Identify the blood parasite species.
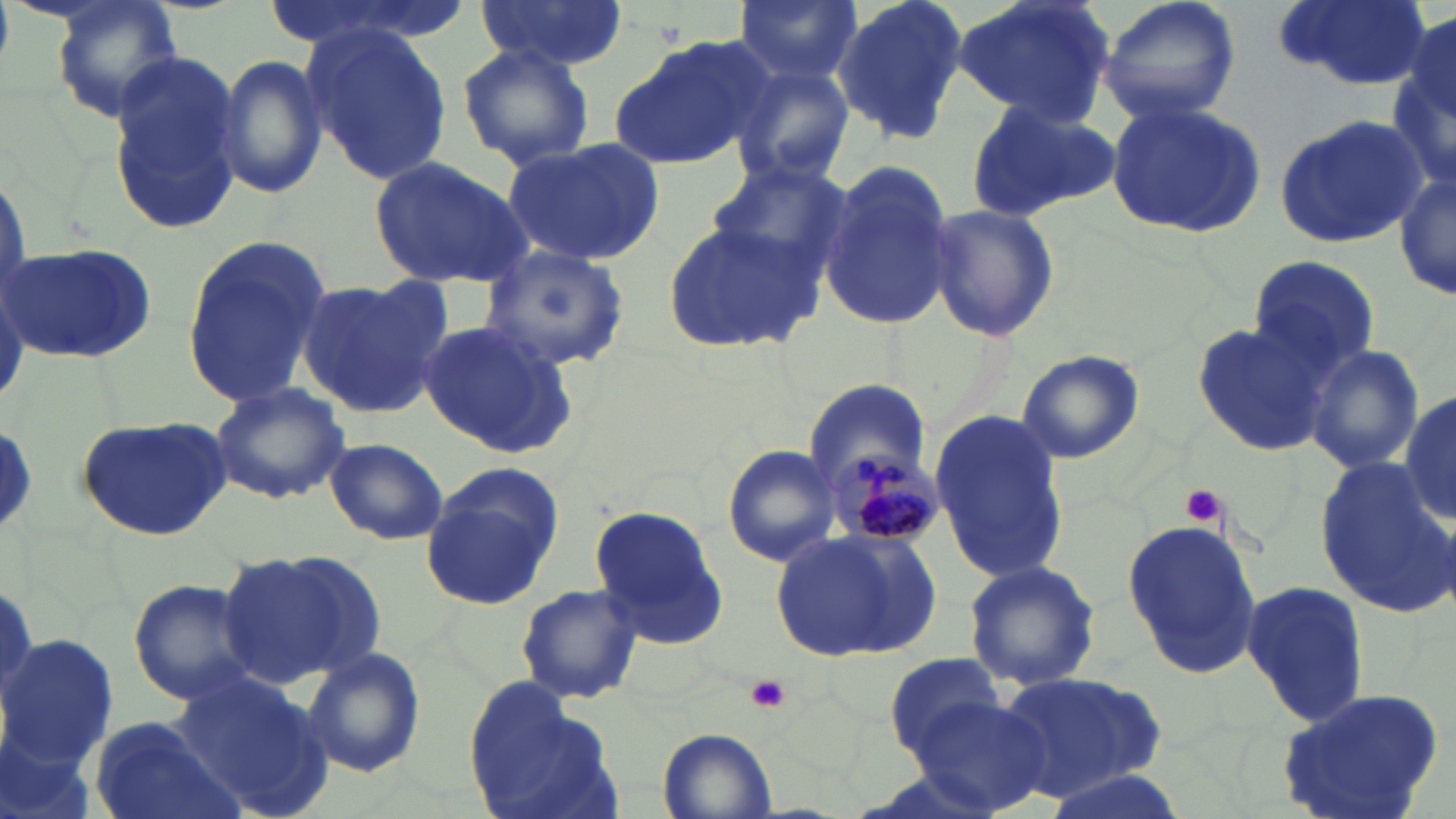

Plasmodium malariae.

platelet_locations: 'approximate bounding boxes as named x1/y1/x2/y2 corners in pixels: (x1=1180, y1=483, x2=1230, y2=528), (x1=746, y1=674, x2=792, y2=715)'
preparation: thin blood film
plasmodium_malariae_infected_red_blood_cell_locations: 'approximate bounding boxes as named x1/y1/x2/y2 corners in pixels: (x1=830, y1=453, x2=940, y2=549)'
modality: light microscopy
stain: May-Grünwald-Giemsa
image_size: 1456×819 pixels
field_of_view: one of a larger specimen
uninfected_red_blood_cell_locations: 'approximate bounding boxes as named x1/y1/x2/y2 corners in pixels: (x1=50, y1=0, x2=185, y2=124), (x1=265, y1=0, x2=466, y2=55), (x1=476, y1=0, x2=630, y2=69), (x1=732, y1=0, x2=862, y2=85), (x1=835, y1=0, x2=969, y2=144), (x1=951, y1=0, x2=1117, y2=127), (x1=1098, y1=0, x2=1242, y2=125), (x1=1273, y1=0, x2=1433, y2=90), (x1=1401, y1=11, x2=1456, y2=128), (x1=301, y1=21, x2=453, y2=187), (x1=608, y1=33, x2=772, y2=171), (x1=457, y1=42, x2=594, y2=172), (x1=109, y1=51, x2=246, y2=237), (x1=215, y1=56, x2=331, y2=199), (x1=728, y1=59, x2=855, y2=185), (x1=1388, y1=59, x2=1455, y2=204), (x1=1102, y1=97, x2=1267, y2=236), (x1=964, y1=98, x2=1117, y2=222), (x1=1275, y1=116, x2=1431, y2=249), (x1=498, y1=136, x2=664, y2=267), (x1=368, y1=155, x2=534, y2=286), (x1=705, y1=158, x2=850, y2=287), (x1=816, y1=162, x2=956, y2=332), (x1=1394, y1=176, x2=1455, y2=299), (x1=922, y1=204, x2=1060, y2=342), (x1=661, y1=216, x2=818, y2=355), (x1=178, y1=234, x2=331, y2=412), (x1=4, y1=241, x2=159, y2=361), (x1=480, y1=244, x2=631, y2=371), (x1=1246, y1=255, x2=1382, y2=377), (x1=296, y1=273, x2=453, y2=418), (x1=418, y1=319, x2=582, y2=460), (x1=1192, y1=321, x2=1333, y2=458), (x1=1304, y1=344, x2=1424, y2=473), (x1=1015, y1=351, x2=1145, y2=463), (x1=208, y1=380, x2=350, y2=504), (x1=803, y1=380, x2=933, y2=494), (x1=1399, y1=384, x2=1455, y2=530), (x1=928, y1=410, x2=1068, y2=585), (x1=75, y1=414, x2=233, y2=541), (x1=326, y1=438, x2=449, y2=545), (x1=721, y1=443, x2=843, y2=568), (x1=1314, y1=454, x2=1456, y2=617), (x1=422, y1=469, x2=560, y2=609), (x1=588, y1=505, x2=731, y2=650), (x1=1120, y1=516, x2=1265, y2=678), (x1=771, y1=525, x2=938, y2=663), (x1=220, y1=549, x2=381, y2=685), (x1=964, y1=560, x2=1102, y2=691), (x1=126, y1=577, x2=263, y2=707), (x1=1240, y1=579, x2=1371, y2=729), (x1=514, y1=582, x2=642, y2=705), (x1=4, y1=633, x2=117, y2=769), (x1=301, y1=646, x2=427, y2=777), (x1=882, y1=653, x2=1012, y2=759), (x1=994, y1=666, x2=1166, y2=800), (x1=169, y1=668, x2=324, y2=817), (x1=462, y1=675, x2=612, y2=819), (x1=1270, y1=687, x2=1450, y2=819), (x1=909, y1=696, x2=1051, y2=815), (x1=87, y1=716, x2=240, y2=819), (x1=657, y1=728, x2=778, y2=819), (x1=1040, y1=768, x2=1191, y2=819)'
magnification: 1000x